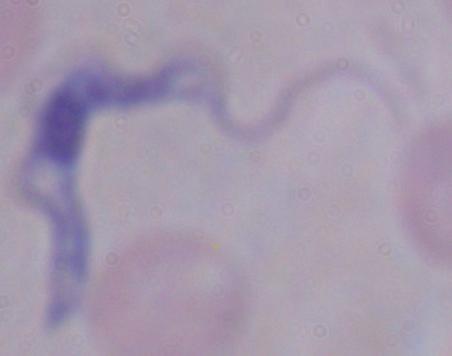 Photomicrograph. A trypanosome is seen. Captured at 1000x magnification.